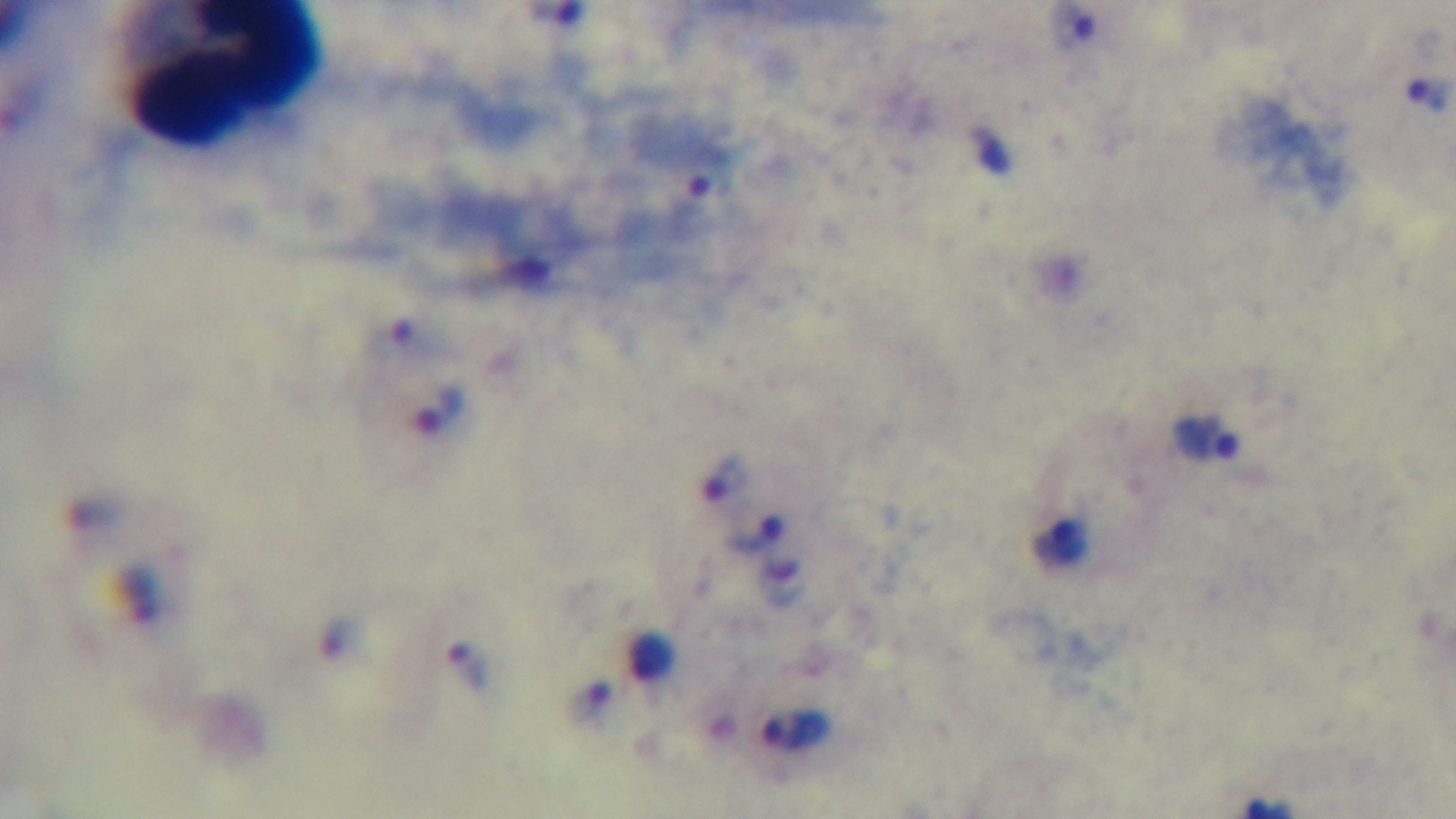
Summary:
  - Capture: mounted 4K digital camera
  - Field of view: one from the slide
  - Objective: 100x oil immersion
  - Stain: Giemsa
  - Malaria status: positive
  - Modality: light microscopy
  - Preparation: thick